Assess this cell for malaria.
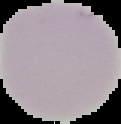

Uninfected.

image size = 121×124 pixels
image type = segmented cell region on a black background
preparation = thin blood film